Locate every parasitized red blood cell.
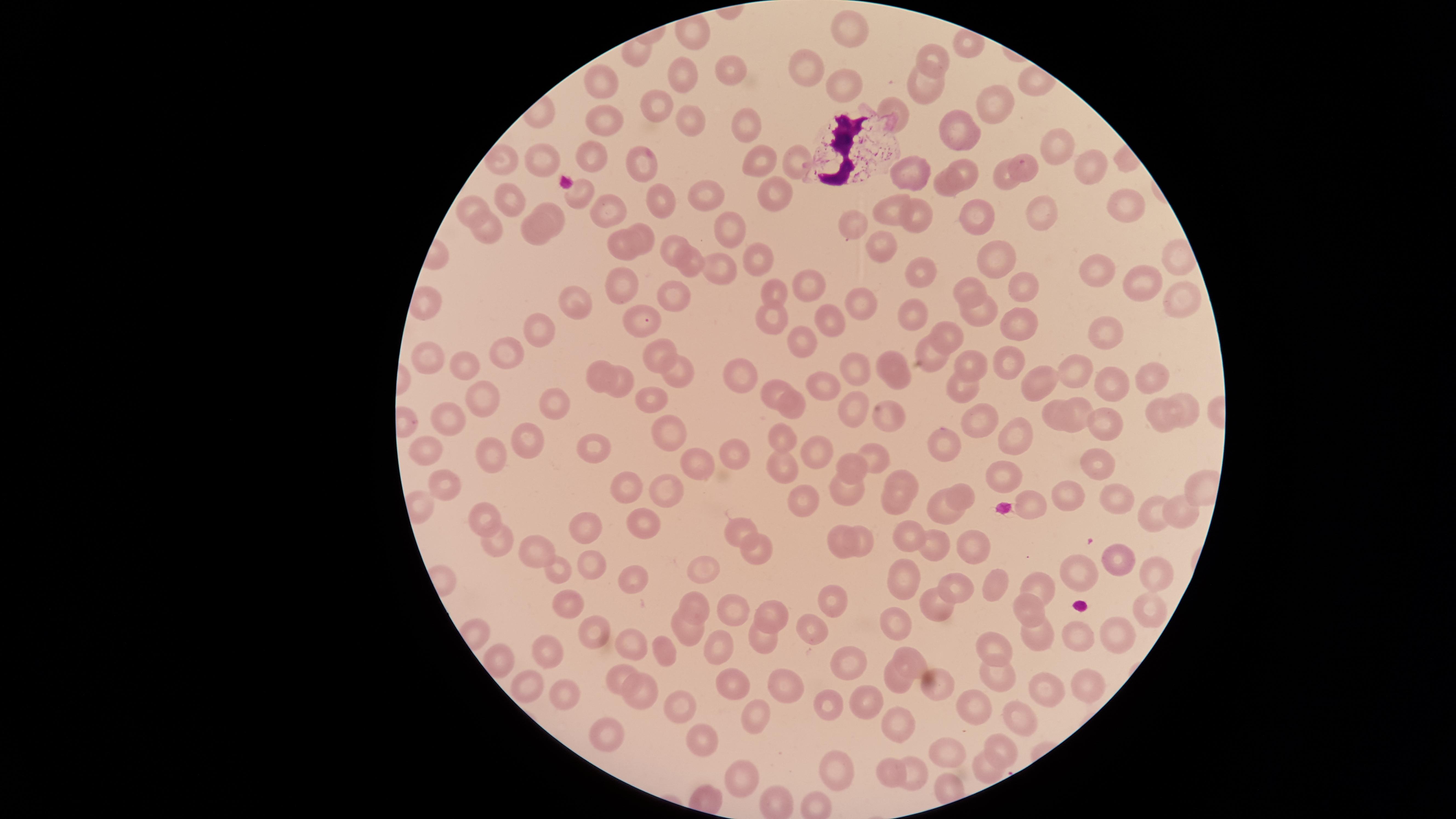

Approximate marker points as [x, y] in pixels.
Parasitized red blood cells: [1022, 163].

Approximate marker points as [x, y] in pixels. Uninfected red blood cells: [849, 24], [938, 57], [810, 63], [727, 73], [680, 74], [605, 77], [836, 78], [923, 86], [658, 104], [999, 105], [899, 113], [601, 116], [689, 125], [752, 127], [963, 128], [596, 155], [499, 157], [647, 158], [752, 160], [540, 161], [796, 163], [1085, 163], [970, 167], [915, 170], [1002, 180], [573, 188], [770, 190], [945, 190], [502, 193], [700, 194], [652, 197], [471, 203], [1121, 204], [602, 205], [891, 208], [924, 209], [553, 210], [1042, 212], [975, 214], [724, 225], [856, 226], [483, 227], [642, 230], [535, 232], [662, 241], [621, 246], [878, 248], [761, 259], [1001, 260], [693, 266], [716, 266], [1096, 271], [923, 274], [1145, 278], [807, 281], [1029, 286], [967, 287], [622, 291], [666, 291], [772, 291], [1174, 294], [855, 304], [578, 309], [980, 310], [911, 316], [830, 318], [1021, 320], [777, 321], [641, 322], [948, 329], [1101, 330], [544, 333], [802, 341], [657, 346], [504, 350], [427, 354], [925, 359], [974, 360], [1008, 362], [887, 364], [850, 367], [466, 368], [679, 370], [740, 370], [1075, 372], [593, 373], [1153, 375], [626, 379], [827, 382], [1112, 386], [774, 389], [960, 389], [1039, 389], [654, 396], [554, 400], [1187, 401], [851, 403], [489, 404], [1080, 404], [794, 405], [891, 414], [1055, 416], [1160, 419], [976, 420], [453, 421], [1106, 427], [675, 435], [784, 436], [1020, 436], [525, 441], [945, 441], [597, 445], [426, 448], [734, 450], [816, 454], [486, 455], [873, 455], [694, 457], [1094, 460], [853, 467], [784, 470], [1002, 471], [905, 477], [442, 482], [633, 487], [669, 487], [849, 490], [961, 490], [1114, 497], [1073, 498], [803, 500], [1031, 500], [895, 507], [1182, 511], [1153, 512], [941, 513], [482, 514], [642, 515], [585, 519], [744, 525], [862, 531], [907, 535], [500, 540], [941, 543], [968, 546], [754, 547], [842, 548], [539, 550], [1116, 559], [585, 562], [703, 567], [561, 569], [1155, 570], [1082, 572], [637, 579], [903, 580], [996, 584], [962, 585], [1029, 586], [696, 600], [570, 601], [831, 604], [1153, 605], [935, 608], [1031, 609], [729, 610], [771, 610], [898, 620], [686, 625], [600, 630], [809, 630], [1038, 631], [1077, 634], [759, 639], [1116, 639], [995, 643], [633, 645], [716, 649], [913, 653], [548, 654], [666, 654], [497, 660], [846, 662], [999, 675], [532, 677], [615, 677], [731, 685], [782, 685], [897, 685], [954, 686], [1091, 686], [1047, 689], [632, 692], [567, 696], [866, 698], [834, 703], [968, 704], [677, 709], [757, 715], [1011, 715], [906, 725], [608, 739], [705, 741], [999, 742], [946, 749], [920, 760], [987, 766], [839, 768], [890, 773], [745, 774], [777, 799]. White blood cells: [854, 149]. Image is 1456×819 pixels. Thin blood film. Circular visible region. Giemsa stain. Smartphone photograph through the microscope eyepiece. Species: Plasmodium falciparum. Single field of view.